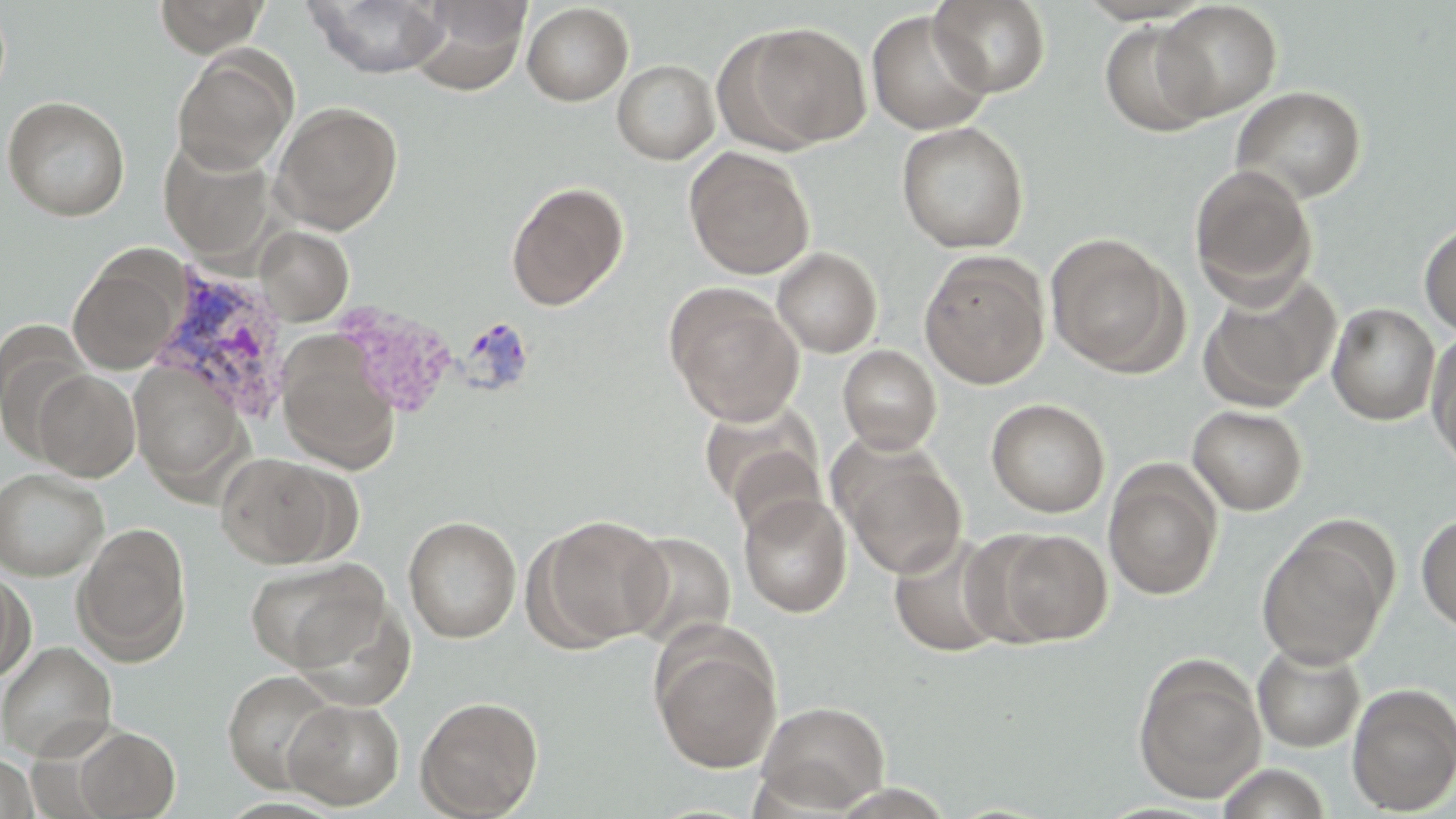
slide_level_diagnosis: Plasmodium vivax
field_of_view: single
plasmodium_vivax_infected_red_blood_cell_locations: 'approximate bounding boxes as named x1/y1/x2/y2 corners in pixels: (x1=150, y1=265, x2=293, y2=426)'
preparation: thin blood smear
image_size: 1456×819 pixels
stain: May-Grünwald-Giemsa
uninfected_red_blood_cell_locations: 'approximate bounding boxes as named x1/y1/x2/y2 corners in pixels: (x1=154, y1=0, x2=268, y2=56), (x1=409, y1=0, x2=531, y2=95), (x1=929, y1=0, x2=1052, y2=97), (x1=305, y1=1, x2=449, y2=79), (x1=1154, y1=1, x2=1283, y2=120), (x1=522, y1=3, x2=633, y2=106), (x1=866, y1=10, x2=994, y2=135), (x1=1100, y1=21, x2=1217, y2=136), (x1=732, y1=22, x2=871, y2=150), (x1=172, y1=49, x2=297, y2=175), (x1=612, y1=59, x2=719, y2=164), (x1=1231, y1=85, x2=1367, y2=205), (x1=2, y1=95, x2=131, y2=221), (x1=270, y1=101, x2=403, y2=234), (x1=896, y1=121, x2=1030, y2=253), (x1=158, y1=138, x2=276, y2=262), (x1=684, y1=147, x2=814, y2=279), (x1=1189, y1=164, x2=1317, y2=305), (x1=506, y1=180, x2=629, y2=311), (x1=1419, y1=219, x2=1456, y2=337), (x1=255, y1=226, x2=353, y2=325), (x1=1045, y1=233, x2=1184, y2=375), (x1=772, y1=247, x2=882, y2=358), (x1=68, y1=250, x2=187, y2=375), (x1=919, y1=251, x2=1049, y2=389), (x1=1197, y1=272, x2=1339, y2=411), (x1=665, y1=284, x2=804, y2=425), (x1=1327, y1=302, x2=1441, y2=425), (x1=0, y1=321, x2=93, y2=457), (x1=1426, y1=330, x2=1456, y2=472), (x1=277, y1=340, x2=400, y2=473), (x1=838, y1=345, x2=941, y2=454), (x1=130, y1=362, x2=247, y2=491), (x1=32, y1=369, x2=140, y2=481), (x1=986, y1=398, x2=1110, y2=517), (x1=699, y1=401, x2=825, y2=524), (x1=1187, y1=405, x2=1307, y2=515), (x1=834, y1=443, x2=967, y2=580), (x1=216, y1=452, x2=346, y2=569), (x1=1103, y1=461, x2=1223, y2=601), (x1=0, y1=468, x2=109, y2=580), (x1=738, y1=494, x2=852, y2=617), (x1=1416, y1=513, x2=1456, y2=634), (x1=530, y1=514, x2=671, y2=649), (x1=403, y1=515, x2=521, y2=643), (x1=73, y1=522, x2=192, y2=665), (x1=1255, y1=524, x2=1394, y2=671), (x1=991, y1=529, x2=1112, y2=645), (x1=618, y1=530, x2=736, y2=651), (x1=888, y1=534, x2=1009, y2=658), (x1=244, y1=557, x2=389, y2=674), (x1=0, y1=568, x2=35, y2=682), (x1=291, y1=599, x2=415, y2=712), (x1=652, y1=629, x2=782, y2=773), (x1=0, y1=641, x2=117, y2=761), (x1=1252, y1=642, x2=1365, y2=752), (x1=1132, y1=655, x2=1268, y2=803), (x1=223, y1=670, x2=340, y2=792), (x1=1346, y1=683, x2=1456, y2=815), (x1=415, y1=695, x2=544, y2=818), (x1=283, y1=698, x2=404, y2=810), (x1=755, y1=700, x2=891, y2=814), (x1=73, y1=726, x2=180, y2=817), (x1=0, y1=754, x2=39, y2=819), (x1=1213, y1=763, x2=1334, y2=819)'
modality: optical microscopy
magnification: 1000x